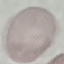

Summary:
  - Result: no malaria parasites detected
  - Capture: smartphone camera at the microscope eyepiece
  - Image type: automatically extracted cell patch, resized to 64 × 64 pixels
  - Stain: Giemsa
  - Preparation: thin blood smear